Comment on the morphology of the erythrocytes.
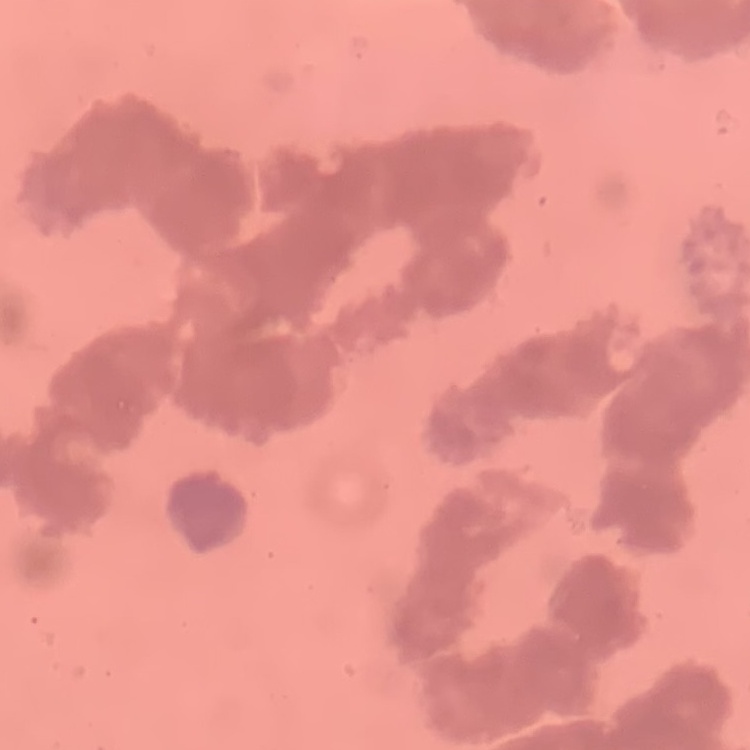
They show rouleaux formation.

Thin peripheral smear. One tile cut from a larger photomicrograph. Field's or Giemsa stain.